Assess this cell for malaria.
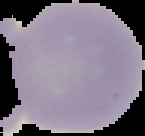
It is uninfected.

Segmented cell region on a black background. Image is 145×136 pixels. From a thin blood film.